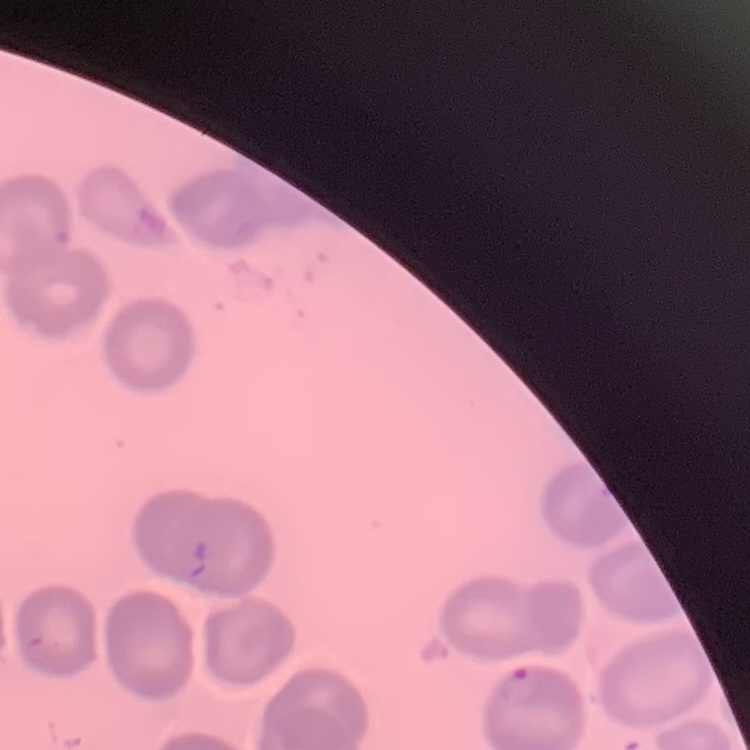

The red blood cells exhibit no rouleaux formation. One tile cut from a larger photomicrograph. Stained with either Field's or Giemsa. Thin peripheral smear.